Outline platelets.
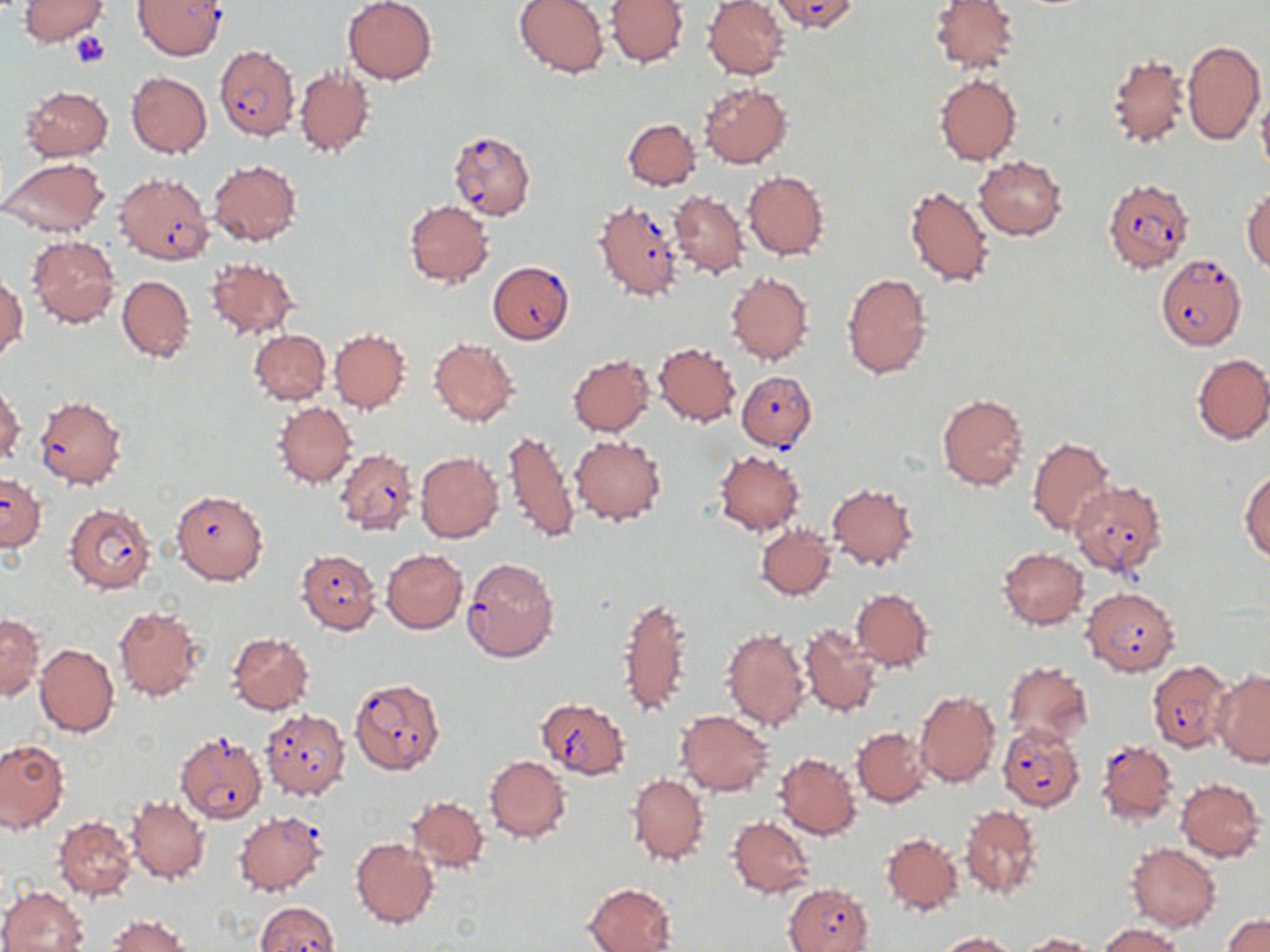

Approximate bounding boxes as (x1, y1, x2, y2) in pixels.
Platelets: (69, 31, 111, 68).

Summary:
  - Uninfected red blood cell locations: (17, 0, 108, 45), (342, 0, 438, 84), (513, 0, 609, 77), (606, 0, 689, 67), (703, 0, 789, 80), (929, 0, 1019, 73), (1182, 39, 1265, 145), (1107, 53, 1190, 148), (294, 66, 374, 158), (126, 71, 211, 158), (933, 74, 1022, 165), (699, 83, 792, 168), (20, 85, 113, 161), (1257, 94, 1270, 178), (623, 118, 700, 191), (973, 154, 1067, 239), (0, 156, 111, 239), (208, 159, 302, 247), (741, 170, 830, 259), (905, 183, 994, 287), (1242, 189, 1270, 271), (669, 191, 749, 278), (404, 200, 493, 287), (27, 236, 121, 327), (205, 257, 298, 340), (841, 271, 932, 380), (725, 272, 814, 365), (0, 274, 26, 362), (116, 275, 194, 363), (248, 329, 330, 405), (329, 330, 409, 412), (428, 338, 519, 426), (653, 342, 741, 426), (567, 354, 654, 436), (1192, 354, 1270, 444), (1, 382, 23, 465), (936, 394, 1029, 490), (274, 401, 356, 488), (503, 428, 578, 546), (570, 434, 666, 525), (1026, 435, 1115, 537), (715, 449, 804, 535), (415, 451, 505, 543), (1240, 469, 1269, 561), (827, 482, 918, 571), (755, 524, 835, 600), (998, 547, 1088, 629), (382, 549, 467, 633), (851, 589, 935, 671), (616, 591, 694, 721), (113, 606, 206, 702), (0, 612, 43, 701), (798, 623, 883, 718), (721, 625, 811, 731), (227, 633, 313, 714), (34, 643, 118, 738), (1004, 661, 1092, 748), (1212, 670, 1270, 766), (914, 689, 1000, 787), (675, 710, 775, 797), (851, 726, 932, 806), (0, 739, 67, 833), (774, 752, 861, 840), (484, 755, 571, 841), (628, 773, 708, 867), (1174, 778, 1265, 861), (125, 796, 209, 884), (407, 796, 489, 872), (959, 805, 1044, 900), (54, 816, 136, 900), (727, 817, 816, 897), (881, 831, 962, 915), (350, 837, 438, 929), (1125, 842, 1221, 931), (583, 882, 678, 952), (0, 885, 89, 952), (1225, 914, 1270, 952), (107, 915, 190, 952), (1097, 922, 1188, 952), (937, 931, 1020, 951), (1020, 933, 1096, 951)
  - Plasmodium falciparum-infected red blood cell locations: (770, 0, 858, 33), (134, 1, 227, 60), (214, 45, 299, 140), (447, 129, 536, 220), (115, 172, 214, 265), (1103, 179, 1194, 272), (593, 200, 684, 302), (1155, 254, 1247, 350), (487, 260, 574, 345), (737, 371, 816, 451), (34, 397, 128, 489), (334, 448, 417, 536), (0, 474, 45, 551), (1068, 480, 1167, 578), (170, 490, 269, 585), (65, 502, 157, 595), (296, 548, 381, 634), (461, 557, 559, 663), (1081, 587, 1182, 676), (1147, 659, 1233, 751), (349, 678, 445, 776), (535, 697, 631, 778), (259, 708, 351, 801), (997, 723, 1086, 812), (175, 731, 267, 823), (1095, 739, 1178, 825), (233, 811, 327, 896), (783, 883, 873, 952), (255, 902, 338, 952)
  - Slide-level diagnosis: Plasmodium falciparum
  - Preparation: thin blood film
  - Image size: 1270×952 pixels
  - Modality: optical microscopy
  - Magnification: 1000x
  - Stain: May-Grünwald-Giemsa
  - Field of view: single